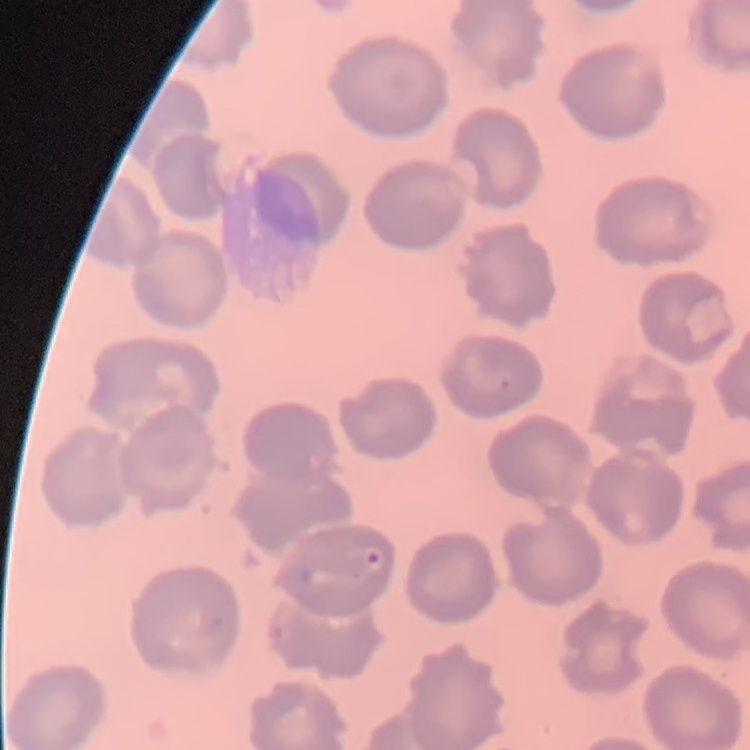

The red blood cells exhibit no rouleaux formation. Field's or Giemsa stain. Thin peripheral smear. Square crop of a larger photomicrograph.